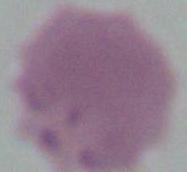

identification = red blood cell
magnification = 1000x
modality = photomicrograph